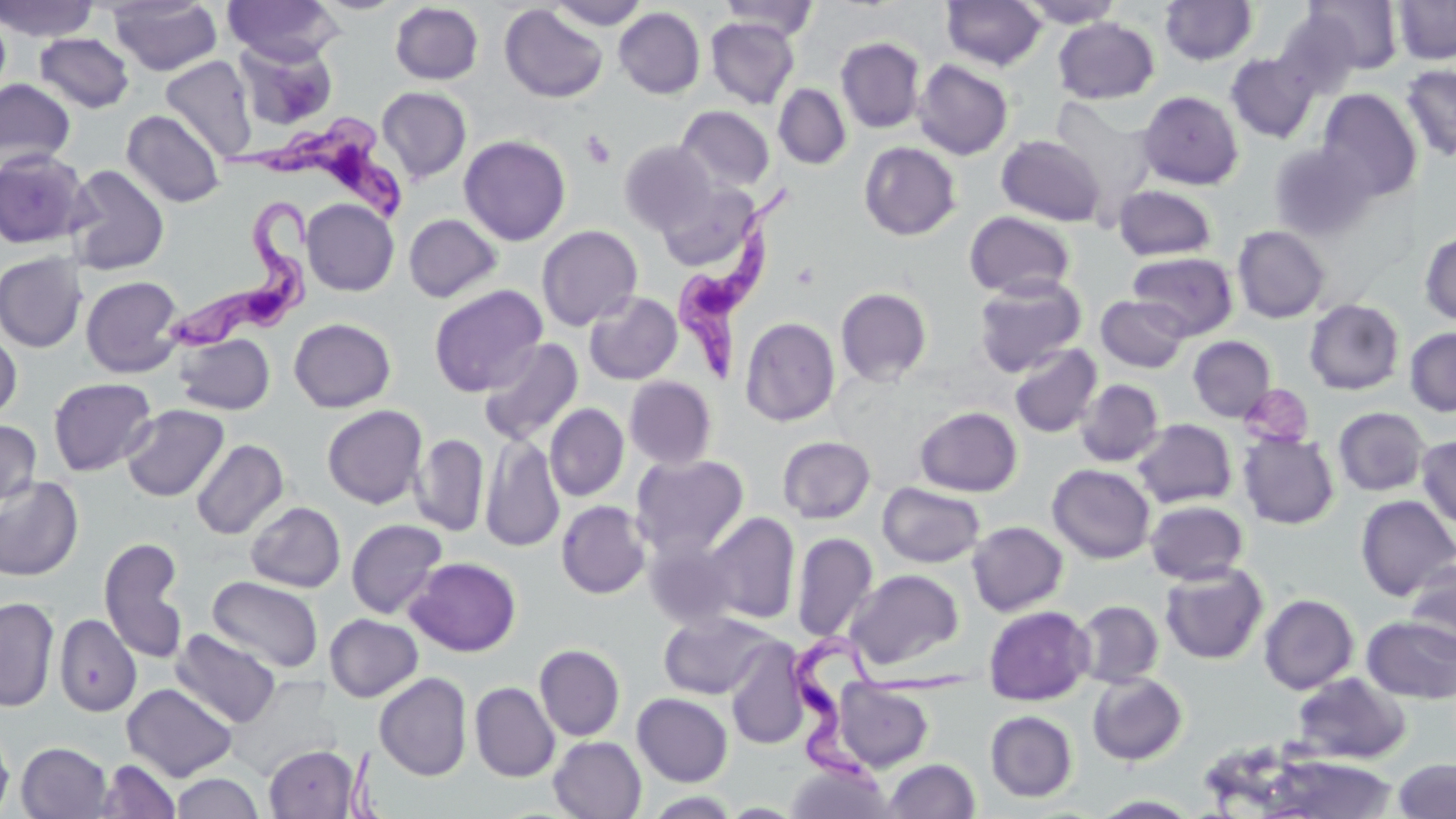

Summary:
  - Coordinate format: approximate bounding boxes as [x1, y1, x2, y2] in pixels
  - Trypanosoma brucei locations: [221, 112, 410, 220], [672, 184, 799, 385], [166, 195, 318, 356], [793, 628, 985, 801]
  - Platelet locations: [581, 131, 616, 168]
  - Uninfected red blood cell locations: [0, 0, 98, 42], [224, 0, 341, 66], [312, 0, 407, 15], [547, 0, 649, 30], [719, 0, 820, 41], [940, 0, 1047, 71], [1019, 0, 1125, 28], [1302, 0, 1404, 74], [1393, 0, 1456, 65], [108, 1, 222, 75], [1160, 1, 1258, 66], [390, 2, 484, 85], [499, 4, 609, 103], [614, 7, 705, 99], [1272, 8, 1363, 97], [1053, 17, 1159, 104], [705, 18, 799, 109], [34, 32, 134, 113], [835, 37, 926, 134], [235, 39, 338, 131], [1226, 52, 1320, 143], [160, 56, 258, 161], [913, 59, 1014, 160], [1400, 64, 1456, 162], [0, 78, 76, 172], [773, 83, 852, 170], [377, 86, 472, 183], [1316, 88, 1422, 202], [1138, 90, 1244, 190], [1050, 97, 1158, 210], [676, 105, 776, 193], [121, 109, 225, 207], [459, 135, 571, 246], [997, 135, 1106, 226], [619, 139, 716, 233], [859, 140, 960, 241], [1269, 143, 1376, 240], [0, 150, 90, 249], [65, 165, 169, 275], [656, 183, 759, 271], [1113, 184, 1217, 261], [301, 199, 399, 296], [964, 211, 1076, 300], [403, 213, 502, 303], [536, 225, 643, 330], [1233, 225, 1331, 323], [1419, 230, 1456, 325], [1127, 251, 1238, 339], [0, 252, 88, 352], [81, 275, 185, 378], [973, 276, 1086, 376], [429, 284, 548, 397], [835, 287, 933, 386], [584, 291, 683, 385], [1096, 295, 1190, 373], [1304, 298, 1405, 395], [739, 316, 840, 427], [289, 318, 396, 412], [0, 327, 23, 423], [1404, 327, 1456, 416], [175, 334, 275, 415], [1187, 335, 1276, 421], [478, 337, 584, 446], [1009, 343, 1102, 438], [624, 376, 717, 469], [48, 377, 157, 476], [1075, 378, 1165, 467], [1240, 384, 1314, 447], [544, 403, 629, 501], [121, 404, 229, 502], [322, 405, 428, 509], [914, 406, 1022, 496], [1333, 407, 1430, 496], [1132, 418, 1237, 508], [0, 419, 42, 508], [1239, 431, 1339, 529], [411, 433, 489, 536], [480, 433, 565, 553], [1416, 434, 1456, 532], [777, 436, 876, 523], [191, 438, 288, 540], [631, 453, 749, 559], [1047, 463, 1156, 563], [0, 475, 83, 582], [877, 482, 985, 568], [1355, 495, 1456, 601], [556, 500, 652, 600], [1145, 500, 1249, 584], [246, 501, 346, 593], [703, 512, 800, 624], [346, 519, 448, 619], [967, 521, 1068, 616], [791, 532, 879, 643], [98, 536, 189, 663], [644, 537, 744, 631], [405, 557, 522, 657], [1404, 561, 1456, 659], [1158, 562, 1268, 664], [846, 569, 964, 670], [207, 576, 324, 673], [1258, 594, 1359, 694], [0, 596, 60, 711], [1075, 599, 1164, 688], [983, 605, 1095, 706], [658, 611, 778, 699], [54, 614, 141, 716], [324, 614, 422, 702], [1360, 615, 1456, 704], [171, 629, 281, 728], [725, 640, 812, 750], [534, 644, 625, 741], [1087, 672, 1187, 766], [1291, 672, 1411, 764], [374, 673, 473, 780], [833, 679, 934, 772], [469, 681, 559, 782], [121, 683, 238, 782], [632, 693, 733, 786], [985, 710, 1078, 802], [0, 723, 14, 817], [548, 736, 647, 819], [16, 742, 112, 818], [263, 744, 360, 819], [1258, 753, 1399, 817], [883, 758, 981, 818], [1393, 758, 1456, 818], [97, 759, 181, 818], [785, 762, 894, 819], [171, 773, 263, 818], [642, 791, 742, 818], [1090, 794, 1202, 817]
  - Slide-level diagnosis: Trypanosoma brucei
  - Field of view: one of a larger specimen
  - Magnification: 1000x
  - Modality: light microscopy
  - Stain: May-Grünwald-Giemsa
  - Preparation: thin blood smear
  - Image size: 1456×819 pixels